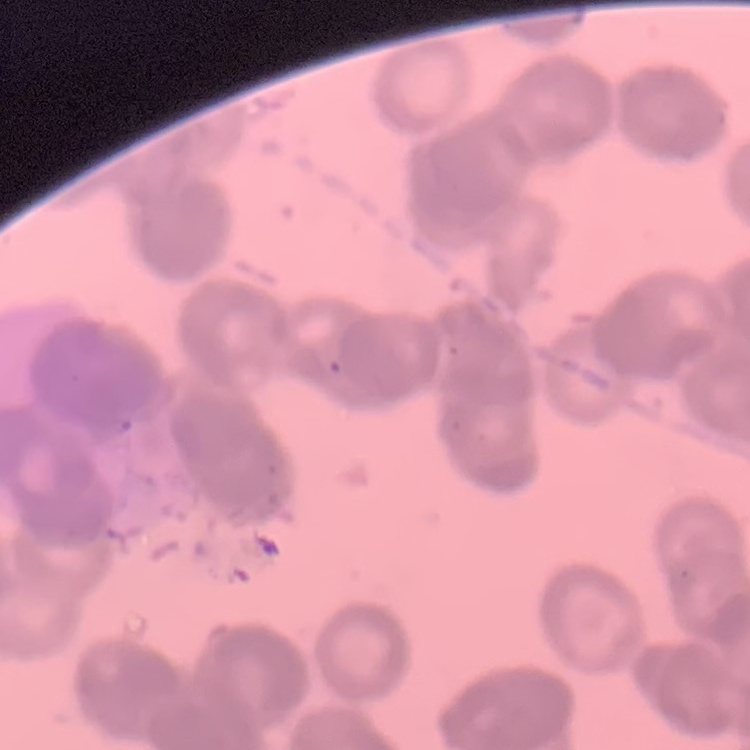

erythrocyte_morphology: rouleaux formation
preparation: thin blood smear
image_type: one tile cut from a larger photomicrograph
stain: Field's or Giemsa